Outline each Trypanosoma brucei.
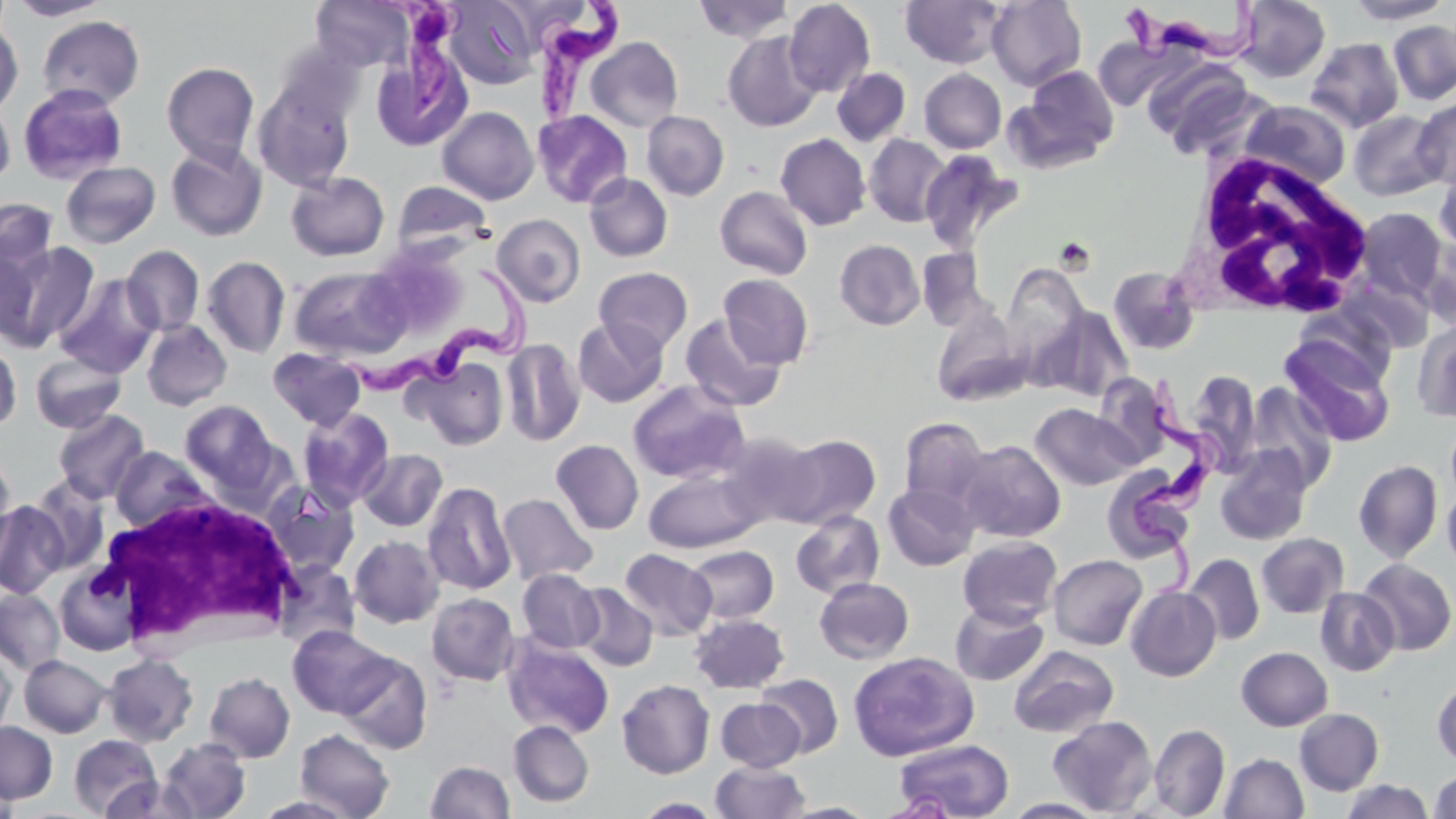
Approximate bounding boxes as [x1, y1, x2, y2] in pixels.
Trypanosoma brucei: [383, 0, 468, 120], [531, 0, 625, 129], [1122, 0, 1264, 69], [343, 262, 528, 408], [1134, 381, 1229, 603].

slide-level diagnosis = Trypanosoma brucei
field of view = one of a larger specimen
platelet locations = approximate bounding boxes as [x1, y1, x2, y2] in pixels: [1054, 237, 1096, 275]
modality = light microscopy
stain = May-Grünwald-Giemsa
preparation = thin blood smear
white blood cell locations = approximate bounding boxes as [x1, y1, x2, y2] in pixels: [1178, 151, 1377, 317], [93, 491, 304, 651]
image size = 1456×819 pixels
uninfected red blood cell locations = approximate bounding boxes as [x1, y1, x2, y2] in pixels: [7, 0, 112, 20], [312, 0, 413, 72], [442, 0, 540, 89], [694, 0, 793, 43], [900, 0, 1006, 69], [988, 0, 1086, 91], [1235, 0, 1331, 82], [1344, 0, 1453, 24], [783, 1, 875, 97], [37, 15, 145, 109], [0, 20, 23, 115], [1388, 20, 1456, 105], [723, 31, 821, 132], [585, 37, 683, 132], [1305, 37, 1405, 133], [371, 43, 473, 153], [1145, 60, 1260, 158], [161, 62, 260, 165], [1016, 66, 1119, 168], [832, 68, 910, 146], [919, 69, 1006, 153], [252, 76, 357, 191], [17, 83, 129, 184], [1412, 98, 1456, 190], [0, 99, 15, 186], [1242, 100, 1351, 190], [437, 106, 539, 205], [532, 110, 633, 208], [1348, 110, 1446, 201], [642, 111, 729, 200], [776, 133, 871, 231], [864, 134, 951, 227], [165, 142, 268, 241], [918, 148, 1022, 253], [61, 161, 161, 248], [1434, 164, 1456, 257], [286, 171, 389, 262], [584, 173, 673, 262], [392, 180, 493, 257], [715, 186, 813, 279], [0, 196, 58, 282], [1352, 207, 1449, 306], [492, 213, 585, 307], [1420, 234, 1456, 332], [1, 239, 99, 352], [835, 239, 924, 330], [121, 245, 204, 336], [917, 247, 988, 330], [201, 256, 290, 358], [1002, 265, 1089, 368], [289, 266, 409, 360], [1108, 266, 1201, 356], [593, 267, 693, 355], [55, 273, 160, 378], [718, 274, 814, 369], [1340, 278, 1435, 353], [1037, 305, 1134, 402], [932, 307, 1027, 406], [680, 314, 785, 412], [572, 317, 668, 407], [141, 320, 232, 411], [1413, 321, 1456, 423], [1281, 336, 1396, 446], [501, 338, 585, 446], [0, 341, 21, 431], [268, 347, 367, 430], [30, 351, 127, 434], [412, 357, 509, 450], [1186, 370, 1260, 473], [627, 380, 749, 484], [1244, 382, 1339, 491], [180, 400, 277, 491], [1030, 403, 1140, 491], [297, 407, 395, 509], [52, 409, 150, 503], [898, 417, 990, 509], [718, 431, 824, 527], [778, 433, 881, 528], [551, 439, 644, 535], [957, 440, 1065, 542], [111, 446, 212, 531], [1214, 447, 1313, 546], [357, 449, 447, 532], [0, 453, 17, 564], [1353, 459, 1442, 562], [1106, 464, 1197, 561], [644, 468, 764, 552], [27, 476, 110, 574], [261, 481, 359, 578], [422, 481, 516, 596], [883, 481, 980, 571], [1442, 485, 1456, 574], [498, 492, 597, 586], [0, 500, 68, 599], [791, 509, 885, 599], [1256, 533, 1349, 618], [349, 535, 444, 628], [958, 536, 1062, 627], [686, 545, 778, 623], [619, 549, 716, 640], [1048, 554, 1147, 650], [1184, 554, 1265, 645], [1358, 559, 1456, 655], [273, 562, 362, 648], [55, 566, 141, 656], [517, 568, 603, 653], [814, 577, 914, 664], [573, 583, 658, 671], [1125, 585, 1221, 681], [1315, 587, 1400, 677], [0, 589, 64, 674], [426, 592, 520, 685], [950, 601, 1049, 686], [689, 613, 789, 693], [288, 625, 392, 718], [502, 636, 614, 739], [1008, 645, 1119, 738], [1237, 646, 1333, 731], [0, 647, 15, 741], [847, 651, 979, 761], [338, 652, 433, 754], [103, 653, 199, 747], [19, 655, 110, 737], [204, 671, 295, 763], [756, 673, 843, 757], [617, 679, 715, 778], [1433, 680, 1456, 767], [716, 698, 804, 771], [1294, 707, 1384, 795], [1048, 715, 1158, 816], [0, 720, 58, 804], [508, 720, 594, 807], [1149, 724, 1230, 817], [294, 728, 395, 818], [69, 734, 162, 817], [158, 738, 251, 819], [894, 738, 1014, 819], [1219, 752, 1309, 818], [425, 760, 514, 819], [710, 761, 810, 818], [1430, 769, 1456, 818], [100, 776, 200, 818], [1341, 779, 1433, 819], [254, 795, 358, 818], [635, 797, 722, 818], [1004, 798, 1108, 818], [780, 801, 879, 818]
magnification = 1000x